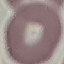 Malaria status: uninfected. Giemsa-stained preparation. Photographed with a smartphone camera at the microscope eyepiece. Cell patch, automatically extracted from a larger field of view and resized to 64 × 64 pixels. Thin smear of blood.